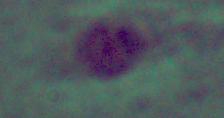

Captured at 1000x magnification. A Leishmania parasite is seen. Photomicrograph.